State which parasite is depicted.
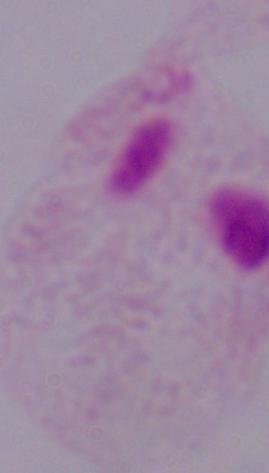
A trichomonad.

Summary:
  - Magnification: 1000x
  - Modality: micrograph